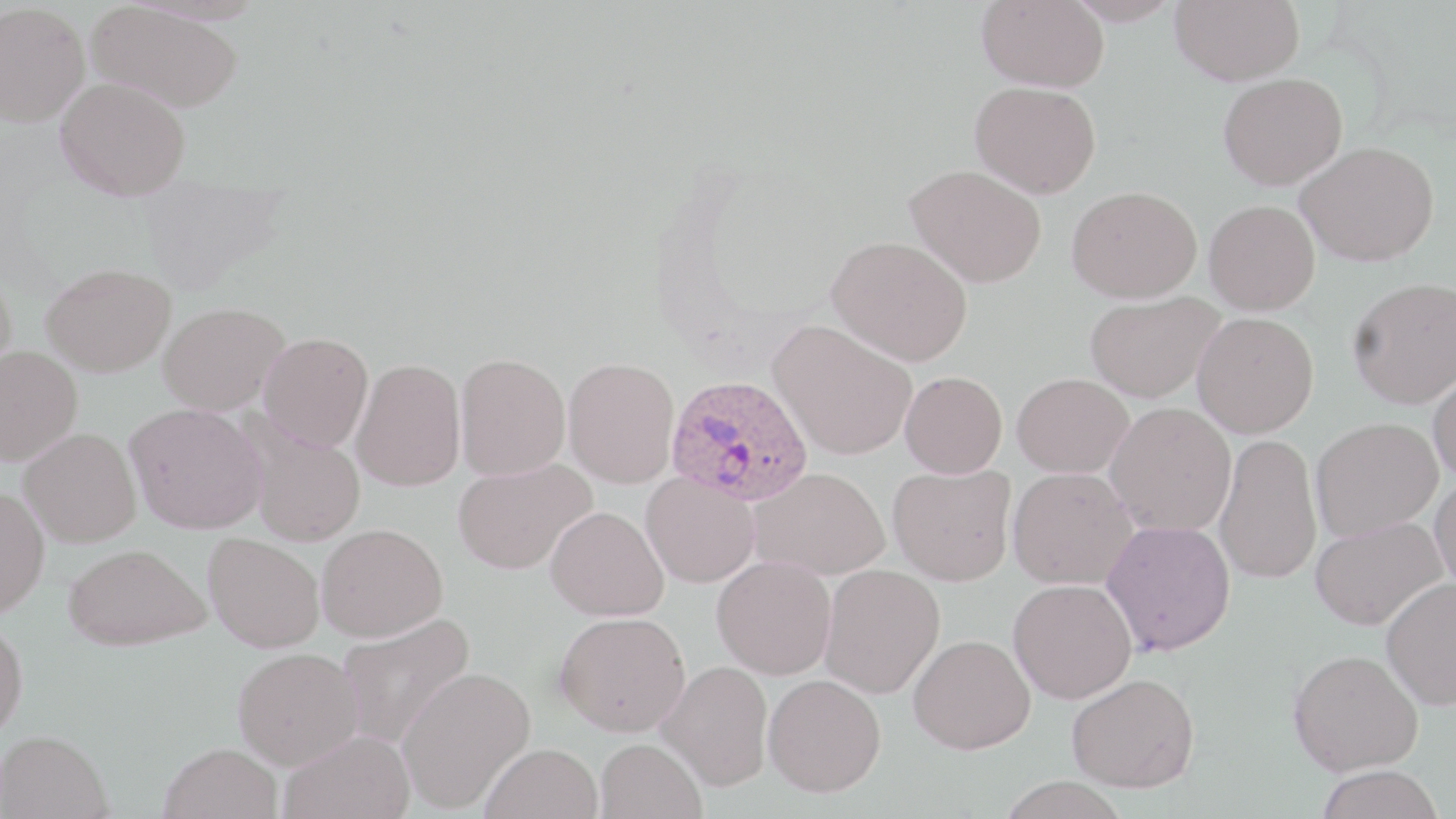
slide-level diagnosis = Plasmodium ovale
field of view = one of a larger specimen
Plasmodium ovale-infected red blood cell locations = approximate bounding boxes as (x1, y1, x2, y2) in pixels: (666, 374, 814, 507)
stain = May-Grünwald-Giemsa
magnification = 1000x
modality = light microscopy
preparation = thin blood smear
image size = 1456×819 pixels
uninfected red blood cell locations = approximate bounding boxes as (x1, y1, x2, y2) in pixels: (977, 0, 1110, 91), (1064, 0, 1183, 27), (1170, 0, 1304, 85), (0, 2, 90, 128), (86, 2, 245, 114), (1218, 73, 1347, 190), (55, 77, 191, 201), (970, 81, 1101, 198), (1296, 141, 1439, 266), (905, 164, 1047, 287), (1066, 186, 1202, 302), (1204, 200, 1320, 315), (827, 235, 973, 366), (41, 262, 176, 376), (0, 268, 17, 387), (1347, 277, 1456, 408), (1084, 291, 1225, 403), (157, 302, 290, 415), (1192, 312, 1318, 438), (768, 319, 917, 461), (258, 332, 374, 452), (0, 345, 82, 465), (454, 352, 570, 481), (562, 357, 680, 488), (351, 359, 466, 491), (1428, 363, 1456, 483), (900, 371, 1007, 478), (1012, 372, 1133, 478), (125, 402, 268, 534), (1104, 402, 1236, 537), (1310, 418, 1442, 542), (245, 425, 366, 547), (19, 428, 142, 547), (1214, 434, 1322, 585), (453, 457, 595, 575), (887, 463, 1017, 586), (1007, 466, 1139, 590), (749, 467, 890, 580), (641, 473, 759, 588), (1429, 476, 1456, 595), (0, 487, 49, 618), (545, 506, 669, 621), (1310, 516, 1446, 630), (1101, 518, 1235, 656), (316, 523, 447, 642), (203, 533, 324, 652), (63, 542, 209, 650), (712, 556, 836, 680), (819, 564, 945, 699), (1380, 576, 1456, 710), (1008, 578, 1137, 703), (555, 611, 691, 736), (336, 612, 475, 749), (0, 617, 28, 740), (908, 633, 1036, 754), (232, 647, 363, 769), (1288, 648, 1424, 776), (657, 660, 773, 790), (396, 667, 535, 812), (1067, 672, 1200, 793), (764, 674, 886, 797), (279, 729, 415, 819), (0, 730, 113, 819), (596, 737, 707, 819), (159, 742, 283, 819), (480, 742, 603, 819), (1315, 764, 1444, 819)